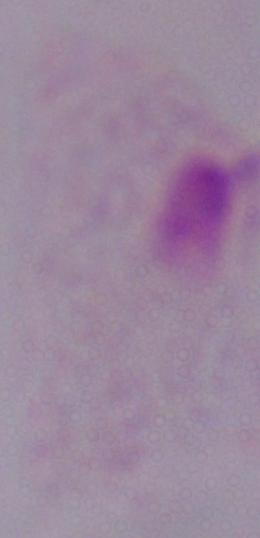

Summary:
  - Magnification: 1000x
  - Modality: photomicrograph
  - Identification: trichomonad